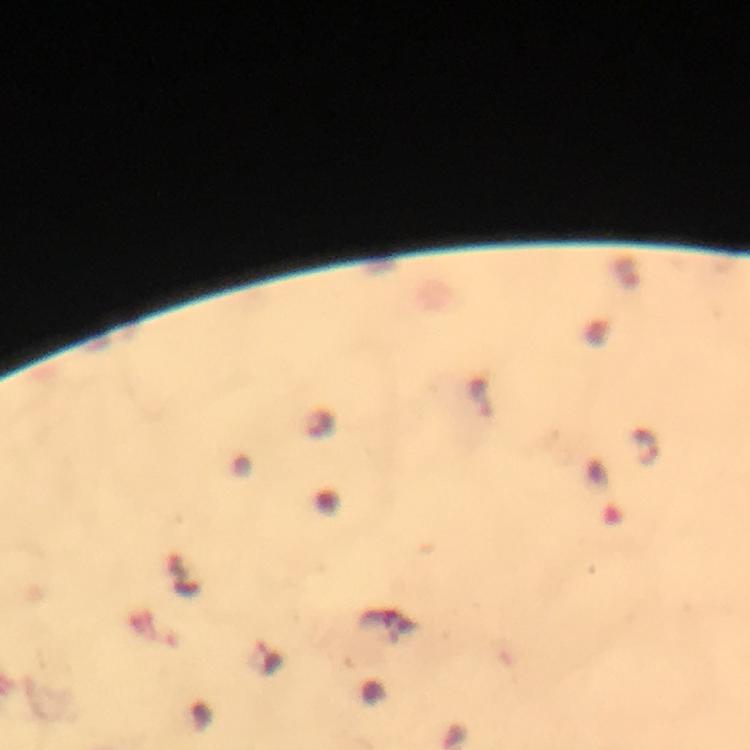

Approximate object centers, in pixels from the top-left corner.
Summary:
  - Malaria parasite locations: (x=645, y=447)
  - Capture: smartphone photograph through a microscope
  - Immersion oil: applied
  - Stain: Giemsa
  - Image size: 750×750 pixels
  - Context: from a malaria diagnostic workup
  - Cropped from: a single field of view
  - Preparation: thick smear
  - Magnification: 100x